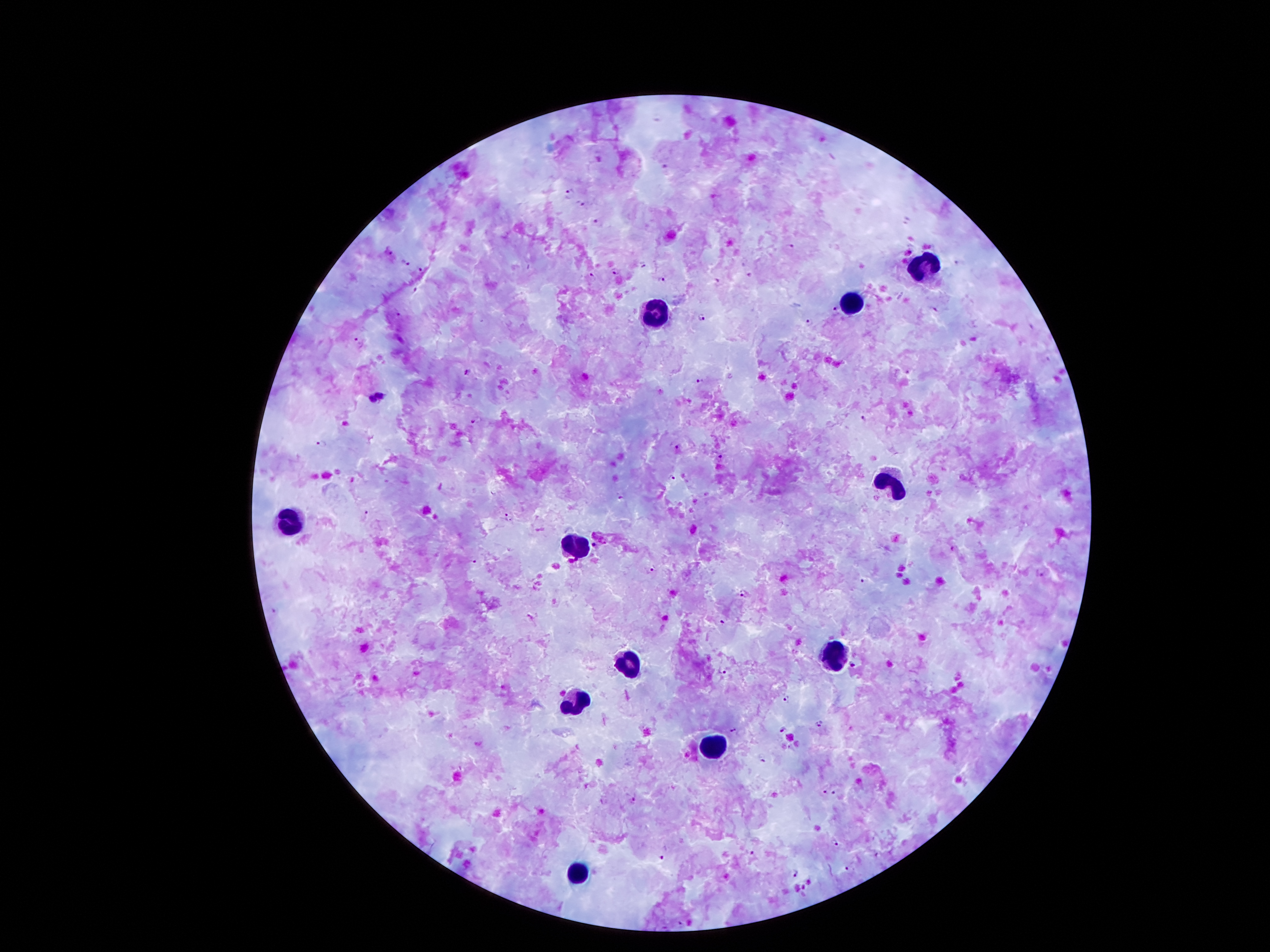
capture: smartphone camera through the microscope eyepiece
malaria_parasite_locations: 'approximate centers as [x, y] in pixels: [665, 166], [570, 190], [583, 203], [597, 221], [791, 246], [389, 252], [404, 262], [643, 264], [954, 264], [421, 269], [615, 271], [592, 273], [749, 276], [662, 281], [718, 283], [416, 290], [933, 310], [835, 311], [398, 314], [703, 316], [808, 321], [1030, 326], [357, 339], [467, 372], [908, 372], [701, 381], [863, 418], [474, 421], [323, 442], [677, 446], [720, 457], [672, 479], [622, 497], [366, 513], [507, 517], [952, 550], [474, 560], [649, 571], [1041, 575], [862, 580], [742, 592], [273, 610], [722, 623], [852, 665], [726, 671], [786, 699], [818, 725], [735, 729], [784, 729], [825, 793], [834, 793], [634, 798], [835, 843], [752, 852], [661, 857], [847, 870], [796, 872], [679, 922]'
preparation: thick peripheral-blood smear
patient_malaria_status: infected with Plasmodium falciparum
magnification: 100x
field_of_view: one from this slide
image_size: 1270×952 pixels
leukocyte_locations: 'approximate centers as [x, y] in pixels: [926, 269], [851, 295], [656, 314], [889, 486], [292, 522], [582, 543], [836, 652], [630, 662], [574, 704], [714, 748], [575, 873]'
stain: Giemsa